Locate every Plasmodium parasite.
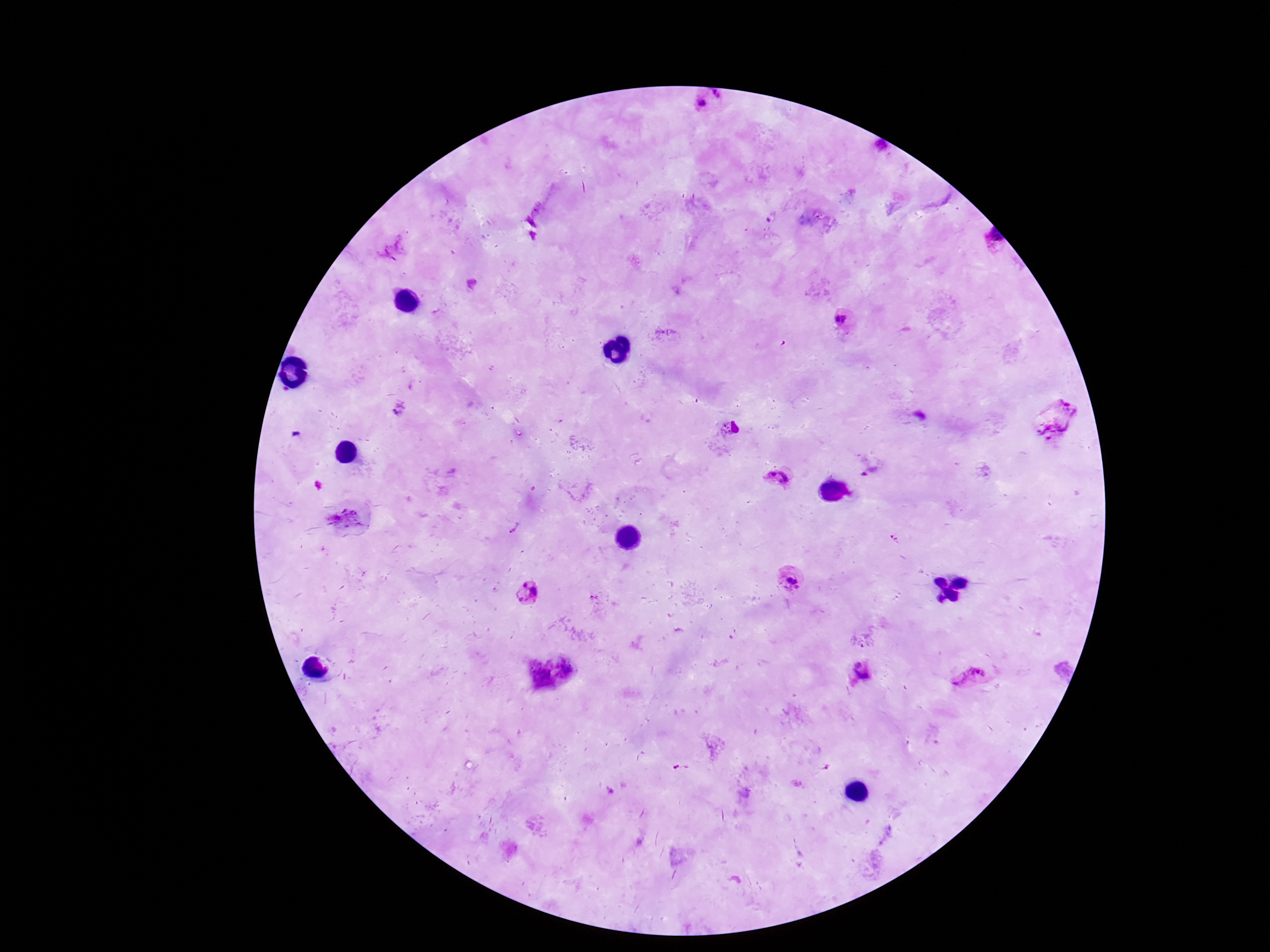
Approximate object centers, in pixels from the top-left corner.
Plasmodium parasites: (x=712, y=100), (x=880, y=148), (x=392, y=250), (x=843, y=319), (x=1057, y=418), (x=780, y=477), (x=895, y=538), (x=791, y=578), (x=529, y=593), (x=862, y=640), (x=862, y=671), (x=971, y=677).

Photographed through the microscope eyepiece with a smartphone camera. Image is 1270×952 pixels. Thick peripheral-blood smear. 100x magnification. One field from this slide. Giemsa stain. Patient malaria status: infected.